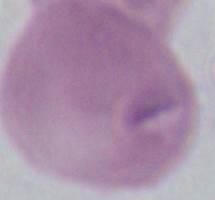

magnification = 1000x
identification = red blood cell
modality = micrograph